Give the extent of all Plasmodium falciparum-infected red blood cells.
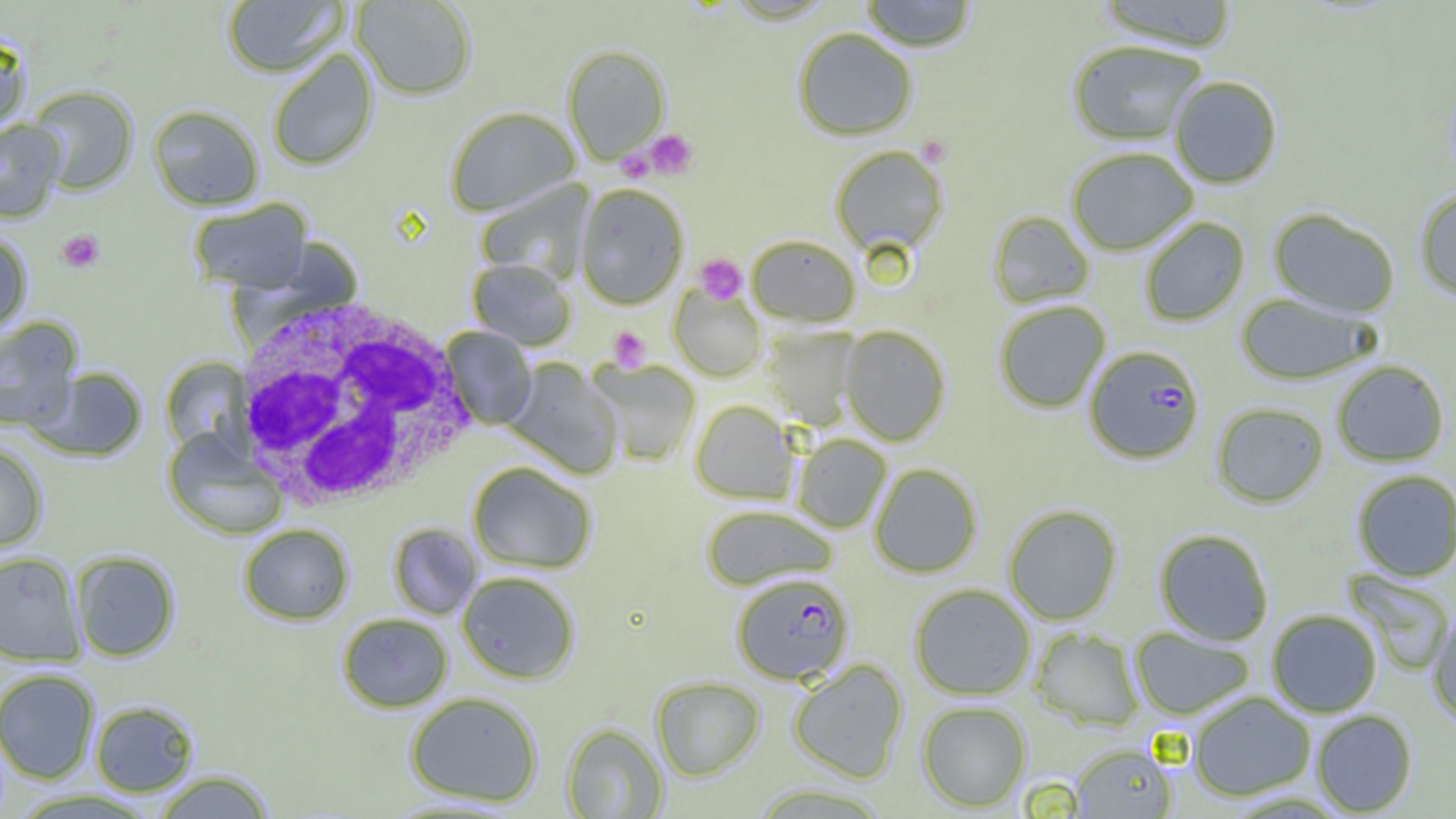

Approximate bounding boxes as (x1,y1)-(x2,y2) corner pairs in pixels.
Plasmodium falciparum-infected red blood cells: (1085,349)-(1206,469), (732,573)-(854,685).

Summary:
  - Uninfected red blood cell locations: (221,0)-(348,77), (351,0)-(477,100), (858,0)-(978,52), (1096,0)-(1239,52), (792,28)-(917,141), (0,30)-(31,130), (1067,40)-(1207,146), (562,45)-(670,164), (267,50)-(378,171), (1169,76)-(1283,189), (28,85)-(138,195), (147,105)-(264,211), (445,107)-(580,217), (0,119)-(65,222), (830,145)-(949,255), (1066,148)-(1198,255), (474,180)-(594,285), (575,184)-(689,309), (1414,188)-(1456,300), (188,198)-(313,293), (1268,208)-(1400,318), (988,211)-(1094,308), (1139,216)-(1250,327), (0,229)-(34,335), (745,235)-(861,327), (468,258)-(576,351), (669,286)-(766,382), (1235,293)-(1376,386), (994,301)-(1110,413), (0,317)-(83,431), (839,324)-(951,446), (440,326)-(537,430), (762,327)-(860,430), (160,358)-(252,456), (504,358)-(622,479), (588,359)-(701,467), (1332,361)-(1449,467), (33,366)-(149,462), (690,400)-(799,504), (1211,403)-(1329,508), (162,428)-(287,541), (792,434)-(892,533), (0,442)-(48,553), (468,462)-(596,574), (869,463)-(982,578), (1351,469)-(1456,582), (701,504)-(837,591), (1003,504)-(1122,626), (237,524)-(354,625), (388,524)-(482,620), (1154,529)-(1274,645), (71,550)-(180,662), (0,551)-(85,666), (456,571)-(580,684), (1345,571)-(1454,676), (909,584)-(1035,700), (1427,607)-(1456,725), (1266,609)-(1382,718), (336,612)-(453,713), (1130,627)-(1254,720), (1030,628)-(1145,731), (788,659)-(908,784), (0,668)-(99,784), (651,676)-(765,781), (404,692)-(543,808), (1188,692)-(1316,802), (89,700)-(200,797), (917,701)-(1031,812), (1311,710)-(1417,817), (561,723)-(668,818), (1071,743)-(1176,818), (151,769)-(276,818), (747,783)-(893,818)
  - Platelet locations: (644,129)-(698,180), (917,135)-(951,167), (617,148)-(655,182), (57,229)-(105,272), (694,254)-(746,305), (608,326)-(651,371)
  - White blood cell locations: (227,295)-(478,513)
  - Slide-level diagnosis: Plasmodium falciparum
  - Image size: 1456×819 pixels
  - Field of view: one of a larger specimen
  - Modality: optical microscopy
  - Preparation: thin blood smear
  - Magnification: 1000x